Give the extent of all Plasmodium falciparum-infected red blood cells.
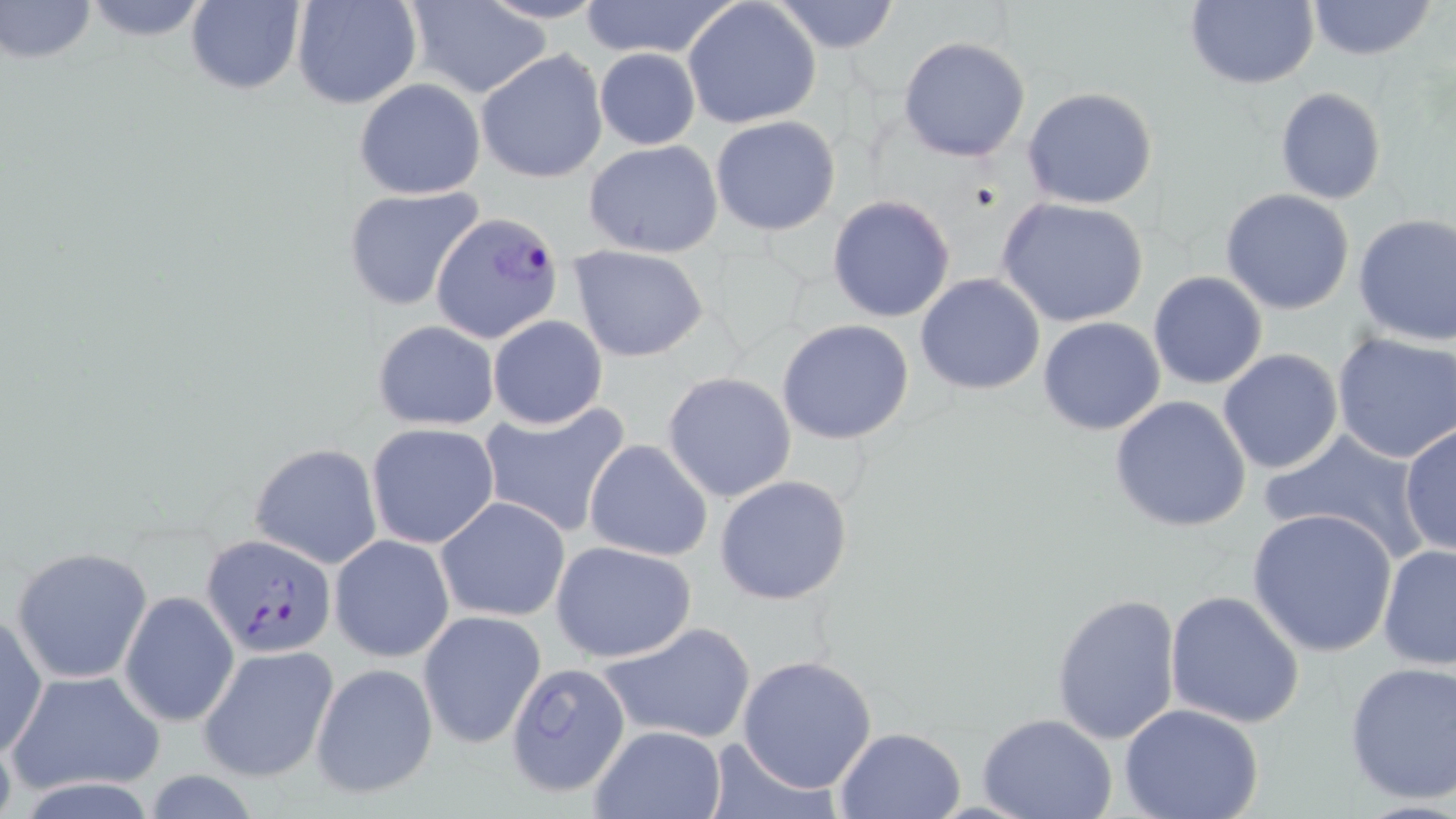

Approximate bounding boxes as [x1, y1, x2, y2] in pixels.
Plasmodium falciparum-infected red blood cells: [433, 212, 566, 345], [202, 533, 337, 658].

Summary:
  - Uninfected red blood cell locations: [1, 0, 99, 65], [76, 0, 217, 41], [184, 0, 306, 95], [290, 0, 422, 110], [769, 0, 901, 53], [1182, 0, 1319, 89], [1305, 0, 1439, 61], [578, 1, 741, 60], [684, 1, 821, 130], [399, 4, 553, 98], [897, 36, 1031, 162], [593, 48, 701, 150], [475, 49, 608, 183], [353, 78, 486, 200], [1022, 87, 1160, 210], [1274, 87, 1388, 205], [710, 115, 841, 236], [584, 140, 725, 258], [341, 186, 484, 312], [1220, 189, 1356, 315], [828, 194, 957, 322], [996, 197, 1149, 327], [1353, 211, 1456, 346], [568, 244, 708, 361], [1148, 270, 1269, 390], [914, 272, 1045, 395], [487, 314, 607, 428], [1038, 317, 1166, 436], [370, 319, 502, 430], [777, 319, 915, 445], [1331, 331, 1456, 464], [1217, 348, 1344, 476], [662, 371, 796, 503], [1108, 395, 1253, 532], [478, 400, 631, 539], [367, 423, 500, 550], [1399, 424, 1455, 557], [1258, 428, 1430, 563], [583, 440, 713, 564], [249, 442, 383, 569], [715, 475, 854, 605], [435, 496, 570, 623], [1248, 508, 1397, 657], [329, 534, 455, 664], [550, 540, 697, 664], [1377, 543, 1456, 669], [10, 546, 152, 685], [120, 590, 240, 726], [1164, 590, 1306, 729], [1049, 592, 1183, 746], [417, 609, 546, 751], [0, 612, 47, 761], [596, 621, 757, 747], [198, 643, 340, 783], [737, 654, 879, 794], [504, 660, 632, 798], [311, 662, 439, 800], [1343, 662, 1456, 804], [7, 669, 165, 798], [1118, 701, 1265, 819], [976, 713, 1118, 819], [588, 725, 728, 819], [833, 726, 966, 818], [700, 737, 844, 819]
  - Slide-level diagnosis: Plasmodium falciparum
  - Modality: light microscopy
  - Field of view: one of a larger specimen
  - Image size: 1456×819 pixels
  - Preparation: thin blood smear
  - Stain: May-Grünwald-Giemsa
  - Magnification: 1000x